Comment on the morphology of the red blood cells.
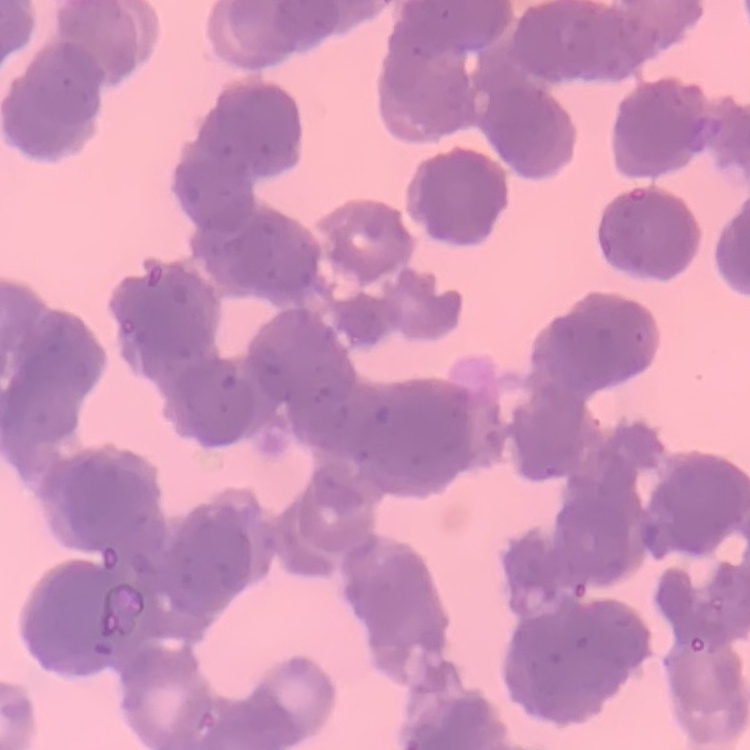

They show rouleaux formation.

Field's or Giemsa stain. Thin blood smear. One tile cut from a larger photomicrograph.